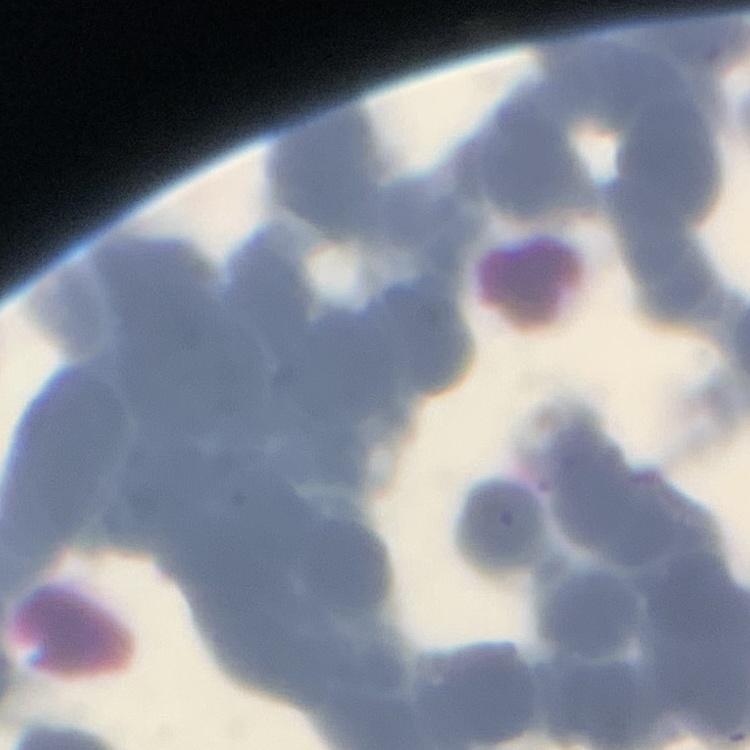
red blood cell morphology = rouleaux formation
preparation = thin blood smear
stain = Field's or Giemsa
image type = square crop of a larger photomicrograph